Assess the morphology of the red blood cells.
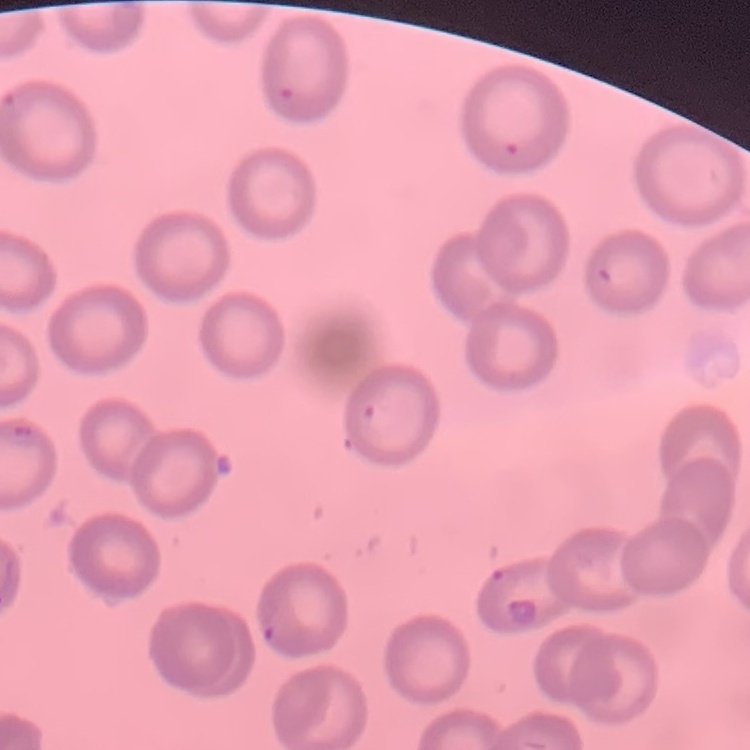
No rouleaux formation.

Summary:
  - Stain: Field's or Giemsa
  - Preparation: thin blood smear
  - Image type: one tile cut from a larger photomicrograph